Outline each blood parasite and name the species.
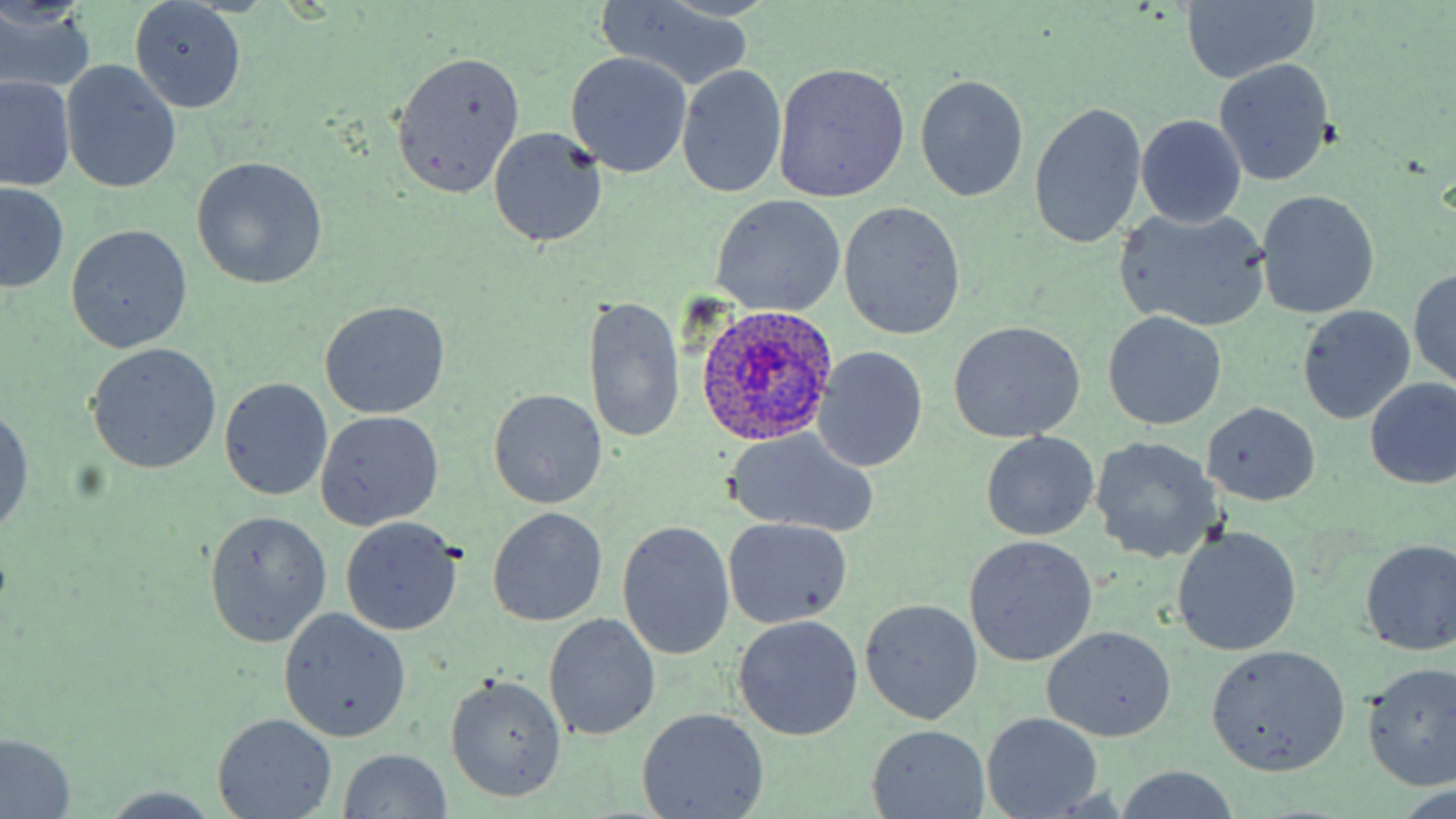
Approximate bounding boxes as (x1,y1)-(x2,y2) corner pairs in pixels.
Plasmodium ovale-infected red blood cells: (695,305)-(840,445).
No Plasmodium falciparum, Plasmodium malariae, Plasmodium vivax, Babesia divergens, or Trypanosoma brucei observed.

Uninfected red blood cell locations: (129,1)-(246,114), (596,1)-(759,90), (1176,1)-(1321,86), (0,3)-(98,96), (392,50)-(526,201), (563,53)-(693,178), (1215,60)-(1334,184), (60,61)-(182,193), (772,62)-(911,202), (676,66)-(787,198), (914,74)-(1029,202), (1,76)-(74,192), (1029,101)-(1147,250), (1135,114)-(1248,228), (488,126)-(606,248), (190,156)-(327,290), (1,183)-(69,292), (1256,192)-(1379,320), (710,195)-(847,317), (838,201)-(966,340), (1114,206)-(1271,333), (65,225)-(193,353), (1410,267)-(1456,392), (583,293)-(685,446), (319,301)-(450,419), (1296,305)-(1415,425), (1102,314)-(1226,428), (947,320)-(1086,443), (84,344)-(223,473), (812,347)-(928,471), (1364,377)-(1456,488), (219,378)-(333,500), (488,389)-(607,508), (1203,401)-(1321,506), (0,405)-(34,537), (314,411)-(444,531), (981,432)-(1099,540), (726,434)-(879,540), (1089,435)-(1222,565), (489,506)-(607,626), (205,511)-(332,648), (340,518)-(462,637), (723,518)-(853,630), (618,519)-(736,659), (1173,528)-(1302,654), (962,535)-(1098,667), (1358,538)-(1456,656), (859,599)-(983,725), (278,609)-(411,742), (544,613)-(661,743), (733,615)-(863,741), (1043,626)-(1175,742), (1206,644)-(1351,777), (1359,662)-(1456,792), (443,674)-(568,803), (636,707)-(769,819), (981,711)-(1104,817), (212,713)-(338,818), (869,726)-(991,816), (0,734)-(76,819), (338,748)-(453,818), (1110,767)-(1242,819), (95,786)-(231,817). Slide-level diagnosis: Plasmodium ovale. Single field of view. Thin blood smear. Optical microscopy. May-Grünwald-Giemsa-stained preparation. Image is 1456×819 pixels. Captured at 1000x magnification.